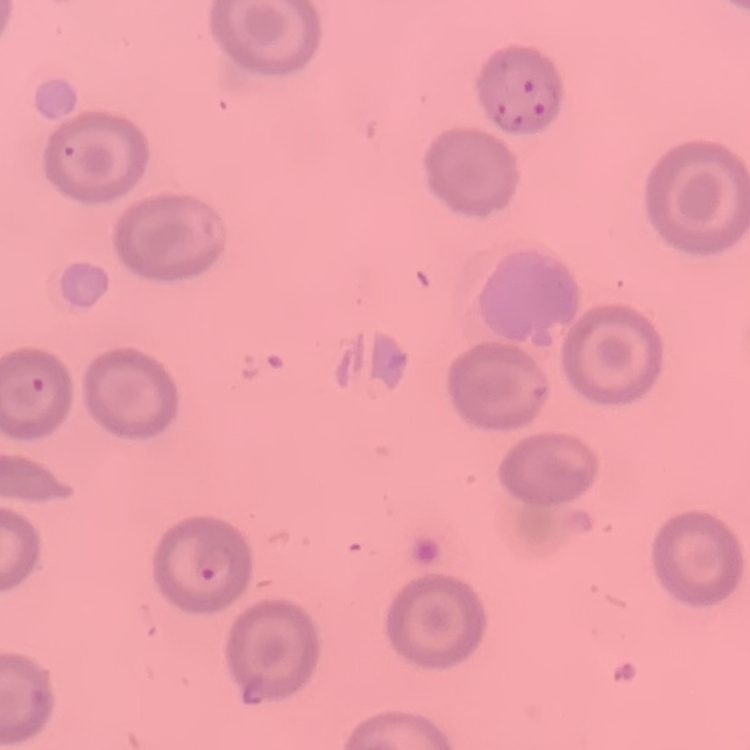

erythrocyte_morphology: no rouleaux formation
image_type: square crop of a larger photomicrograph
stain: Field's or Giemsa
preparation: thin blood film